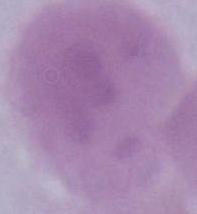
identification = red blood cell
modality = photomicrograph
magnification = 1000x